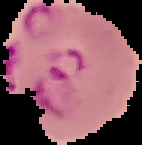
From a thin blood film. Result: malaria parasites detected. Image is 142×145 pixels. The area outside the segmented cell region is set to black.